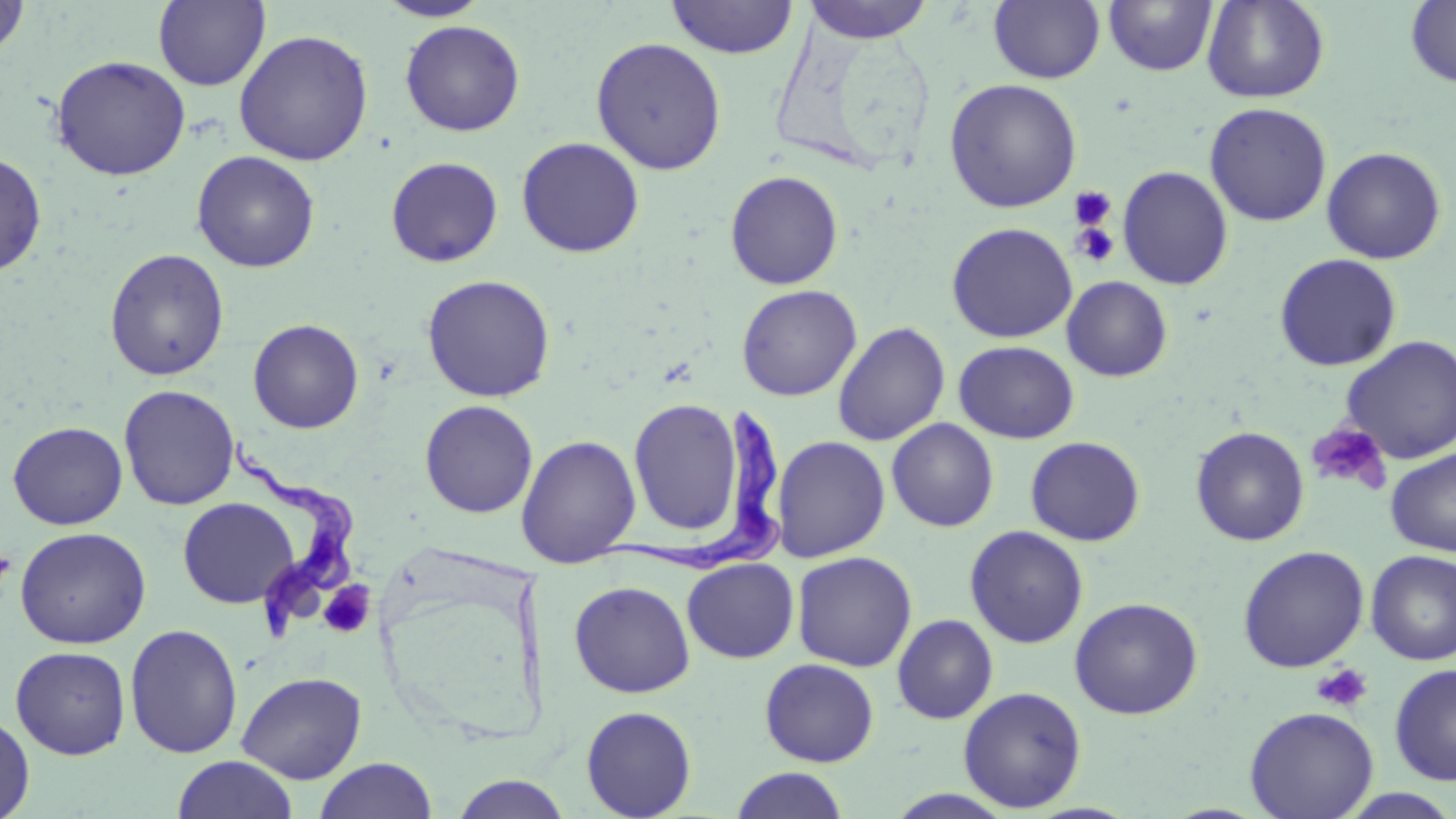 Approximate bounding boxes as (x1, y1, x2, y2) in pixels. Platelet locations: (1069, 186, 1117, 231), (1070, 222, 1120, 268), (1306, 422, 1391, 494), (0, 548, 16, 595), (318, 581, 375, 639), (1311, 663, 1373, 713). Trypanosoma brucei locations: (595, 410, 781, 573), (226, 438, 356, 644). Uninfected red blood cell locations: (0, 0, 32, 60), (375, 0, 492, 22), (666, 0, 799, 59), (801, 0, 936, 43), (1103, 0, 1218, 76), (1202, 0, 1329, 104), (153, 1, 270, 91), (988, 1, 1105, 84), (1405, 1, 1456, 88), (400, 19, 525, 137), (233, 29, 374, 165), (590, 37, 727, 175), (50, 55, 191, 181), (944, 78, 1082, 213), (1204, 102, 1332, 227), (515, 136, 645, 258), (1321, 146, 1447, 265), (191, 150, 320, 273), (0, 151, 47, 276), (385, 156, 504, 268), (1117, 165, 1233, 290), (725, 170, 844, 290), (946, 222, 1077, 343), (104, 248, 230, 381), (1274, 253, 1402, 372), (421, 274, 556, 402), (1061, 275, 1173, 382), (736, 284, 861, 401), (247, 318, 365, 433), (832, 321, 950, 446), (1340, 335, 1456, 464), (953, 340, 1080, 443), (119, 384, 239, 510), (628, 398, 744, 537), (420, 400, 539, 518), (886, 418, 999, 532), (7, 421, 128, 530), (1190, 425, 1310, 546), (515, 434, 641, 568), (771, 435, 891, 562), (1025, 436, 1146, 546), (1386, 448, 1456, 557), (177, 497, 300, 609), (964, 525, 1089, 648), (14, 526, 151, 649), (1238, 545, 1370, 673), (1365, 550, 1456, 665), (791, 551, 917, 671), (682, 557, 799, 663), (569, 581, 695, 698), (1069, 596, 1203, 719), (892, 615, 998, 724), (124, 623, 243, 759), (10, 646, 131, 759), (759, 658, 879, 767), (1389, 662, 1456, 786), (236, 671, 367, 784), (957, 686, 1087, 812), (580, 704, 697, 818), (1244, 706, 1379, 819), (0, 711, 35, 818), (171, 755, 299, 819), (313, 757, 438, 819), (728, 767, 852, 819), (449, 774, 573, 818), (884, 789, 1019, 818), (1335, 789, 1456, 819). Slide-level diagnosis: Trypanosoma brucei. Captured at 1000x magnification. Thin blood smear. May-Grünwald-Giemsa stain. Image is 1456×819 pixels. Light microscopy. Single field of view.